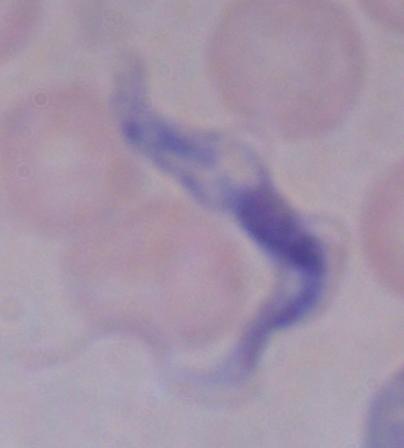 Captured at 1000x magnification. Micrograph. A trypanosome is shown.